Point out every malaria parasite and every leukocyte.
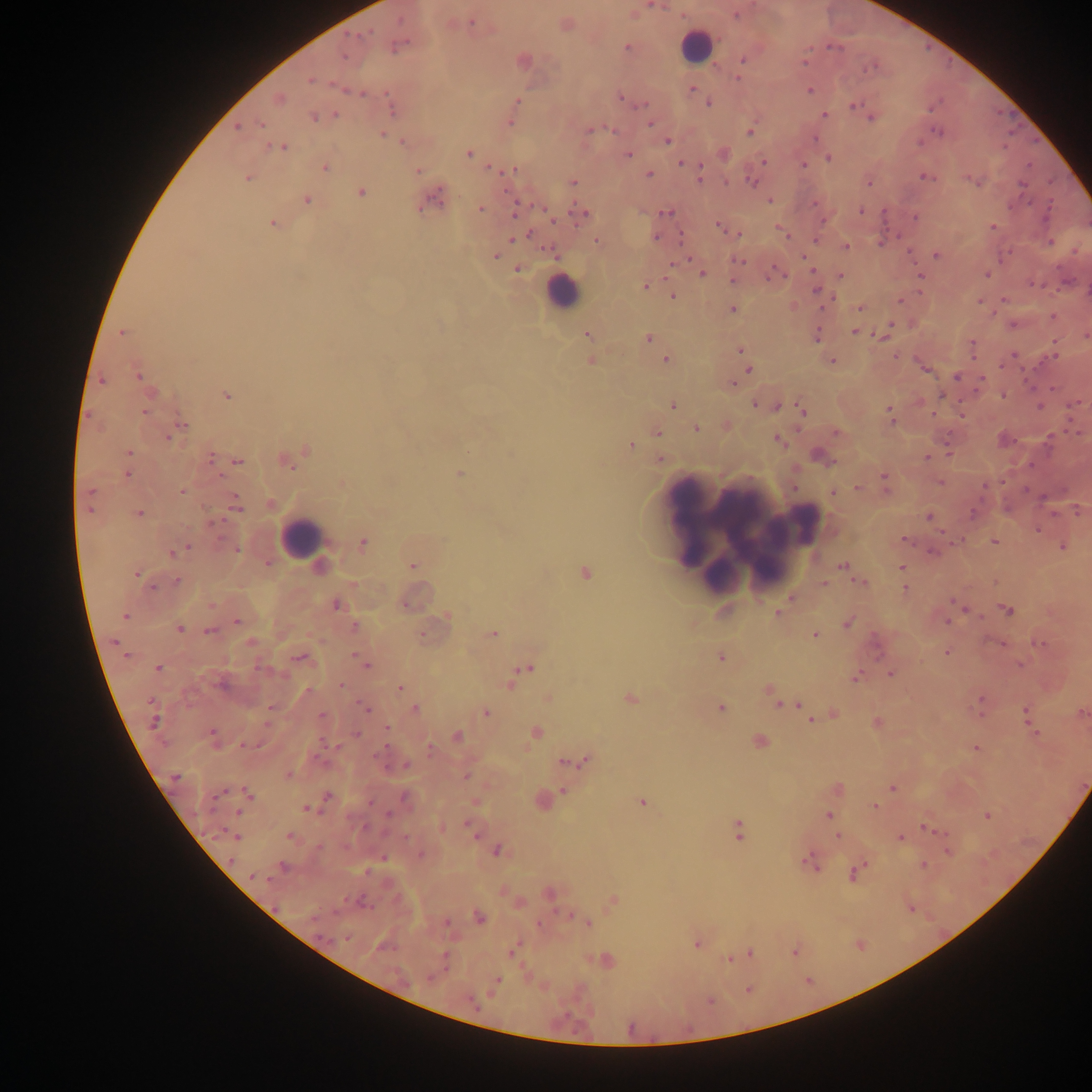
Approximate centers as [x, y] in pixels.
Malaria parasites: [649, 6], [657, 6], [399, 20], [471, 21], [369, 32], [627, 46], [394, 47], [829, 47], [808, 50], [345, 58], [742, 59], [803, 64], [874, 64], [864, 69], [309, 79], [737, 79], [691, 89], [345, 90], [810, 91], [362, 93], [386, 93], [620, 96], [517, 100], [708, 102], [643, 104], [853, 105], [334, 114], [824, 114], [313, 116], [870, 118], [509, 122], [261, 125], [649, 125], [608, 126], [236, 130], [612, 130], [591, 131], [748, 131], [940, 131], [934, 132], [383, 133], [814, 139], [401, 141], [667, 142], [918, 143], [1002, 146], [278, 147], [469, 155], [630, 155], [829, 158], [765, 160], [679, 162], [803, 164], [1029, 165], [700, 166], [488, 167], [324, 168], [515, 169], [417, 171], [649, 173], [924, 176], [248, 179], [698, 180], [971, 180], [574, 182], [727, 182], [753, 182], [867, 182], [1022, 185], [504, 192], [361, 193], [307, 199], [1049, 199], [770, 200], [814, 202], [440, 206], [540, 207], [481, 209], [573, 211], [862, 211], [884, 211], [585, 212], [664, 213], [514, 214], [916, 218], [554, 221], [823, 221], [273, 223], [719, 226], [991, 227], [776, 228], [530, 233], [738, 235], [658, 236], [679, 236], [787, 236], [512, 240], [815, 240], [596, 241], [1050, 241], [881, 244], [846, 247], [545, 249], [910, 251], [1011, 251], [935, 254], [495, 255], [803, 257], [688, 258], [1000, 258], [740, 261], [516, 269], [813, 270], [701, 274], [987, 275], [785, 276], [920, 276], [665, 277], [841, 277], [768, 279], [733, 281], [1030, 282], [644, 286], [1050, 287], [816, 289], [672, 295], [1003, 298], [835, 299], [900, 302], [977, 302], [732, 308], [859, 309], [822, 310], [992, 312], [1052, 318], [891, 323], [855, 331], [120, 332], [1085, 336], [648, 337], [881, 337], [1053, 339], [818, 343], [972, 343], [741, 349], [1014, 355], [895, 356], [1054, 356], [665, 358], [971, 358], [834, 360], [1001, 365], [747, 369], [955, 377], [100, 379], [982, 379], [733, 385], [1030, 385], [1052, 389], [973, 392], [942, 394], [226, 395], [1002, 395], [755, 404], [776, 405], [1073, 405], [672, 406], [1039, 406], [889, 407], [801, 410], [144, 413], [932, 414], [890, 416], [962, 416], [1068, 420], [892, 422], [183, 425], [697, 429], [656, 432], [1074, 432], [1050, 437], [167, 438], [777, 439], [1013, 442], [632, 445], [130, 453], [948, 453], [209, 456], [658, 458], [926, 458], [236, 460], [835, 461], [1031, 465], [127, 474], [884, 474], [220, 475], [941, 483], [985, 487], [795, 488], [856, 488], [886, 489], [182, 491], [89, 492], [235, 495], [237, 508], [91, 511], [139, 513], [974, 513], [1076, 513], [1053, 515], [928, 516], [1039, 530], [941, 531], [220, 538], [904, 538], [963, 540], [994, 541], [188, 546], [1061, 547], [182, 550], [237, 550], [931, 550], [171, 552], [844, 565], [901, 568], [137, 576], [176, 581], [862, 582], [824, 583], [153, 587], [905, 588], [789, 597], [951, 600], [211, 605], [964, 610], [1010, 610], [1013, 611], [778, 612], [127, 617], [979, 618], [237, 621], [947, 622], [846, 624], [180, 629], [209, 632], [813, 634], [115, 640], [251, 644], [1041, 644], [1002, 645], [946, 651], [125, 653], [299, 657], [1019, 664], [259, 665], [366, 665], [158, 667], [284, 674], [891, 674], [856, 676], [341, 685], [400, 688], [768, 690], [309, 692], [979, 698], [629, 699], [778, 704], [798, 705], [269, 707], [363, 707], [414, 707], [719, 707], [1025, 707], [368, 710], [980, 711], [486, 712], [321, 714], [1026, 716], [811, 719], [155, 725], [265, 725], [385, 728], [211, 733], [1035, 733], [357, 734], [535, 734], [322, 744], [241, 745], [385, 746], [975, 746], [430, 750], [563, 761], [404, 763], [289, 775], [177, 777], [243, 788], [891, 788], [224, 790], [562, 790], [327, 796], [251, 797], [371, 802], [875, 807], [305, 808], [239, 812], [388, 815], [827, 815], [988, 815], [466, 824], [737, 827], [923, 828], [943, 833], [475, 836], [836, 836], [289, 837], [236, 838], [900, 838], [737, 839], [318, 846], [498, 850], [947, 852], [386, 857], [232, 860], [804, 862], [864, 864], [923, 865], [366, 871], [852, 874], [251, 878], [267, 879], [502, 892], [569, 915], [480, 918], [445, 922], [539, 924], [590, 924], [346, 940], [696, 945], [510, 952], [445, 956], [728, 959], [498, 978], [470, 1000].
Leukocytes: [697, 42], [559, 292], [743, 530], [298, 533].

Summary:
  - Preparation: thick blood smear
  - Field of view: single
  - Capture: mobile-phone photograph through a microscope
  - Image size: 1092×1092 pixels
  - Country: Ghana